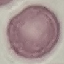

{
  "result": "no malaria parasites seen",
  "preparation": "thin smear",
  "stain": "Giemsa",
  "capture": "smartphone through the microscope eyepiece",
  "image_type": "cell patch, automatically extracted from a larger field of view and resized to 64 × 64 pixels"
}